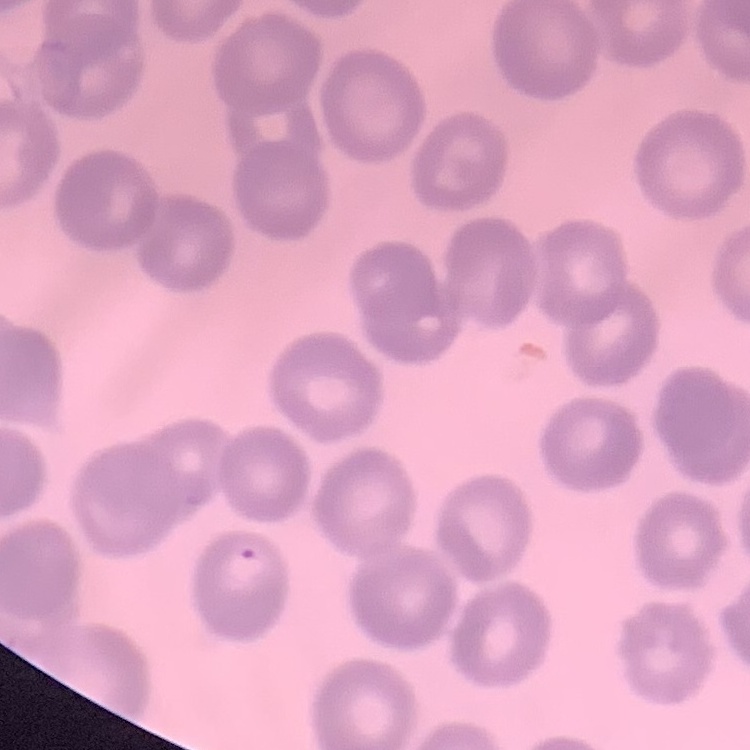
Summary:
  - Erythrocyte morphology: no rouleaux formation
  - Image type: square crop of a larger photomicrograph
  - Preparation: thin blood smear
  - Stain: Field's or Giemsa